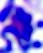

identification = white blood cell
magnification = 400x
modality = micrograph